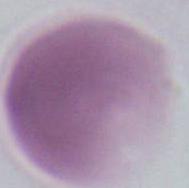

modality = micrograph
magnification = 1000x
identification = red blood cell